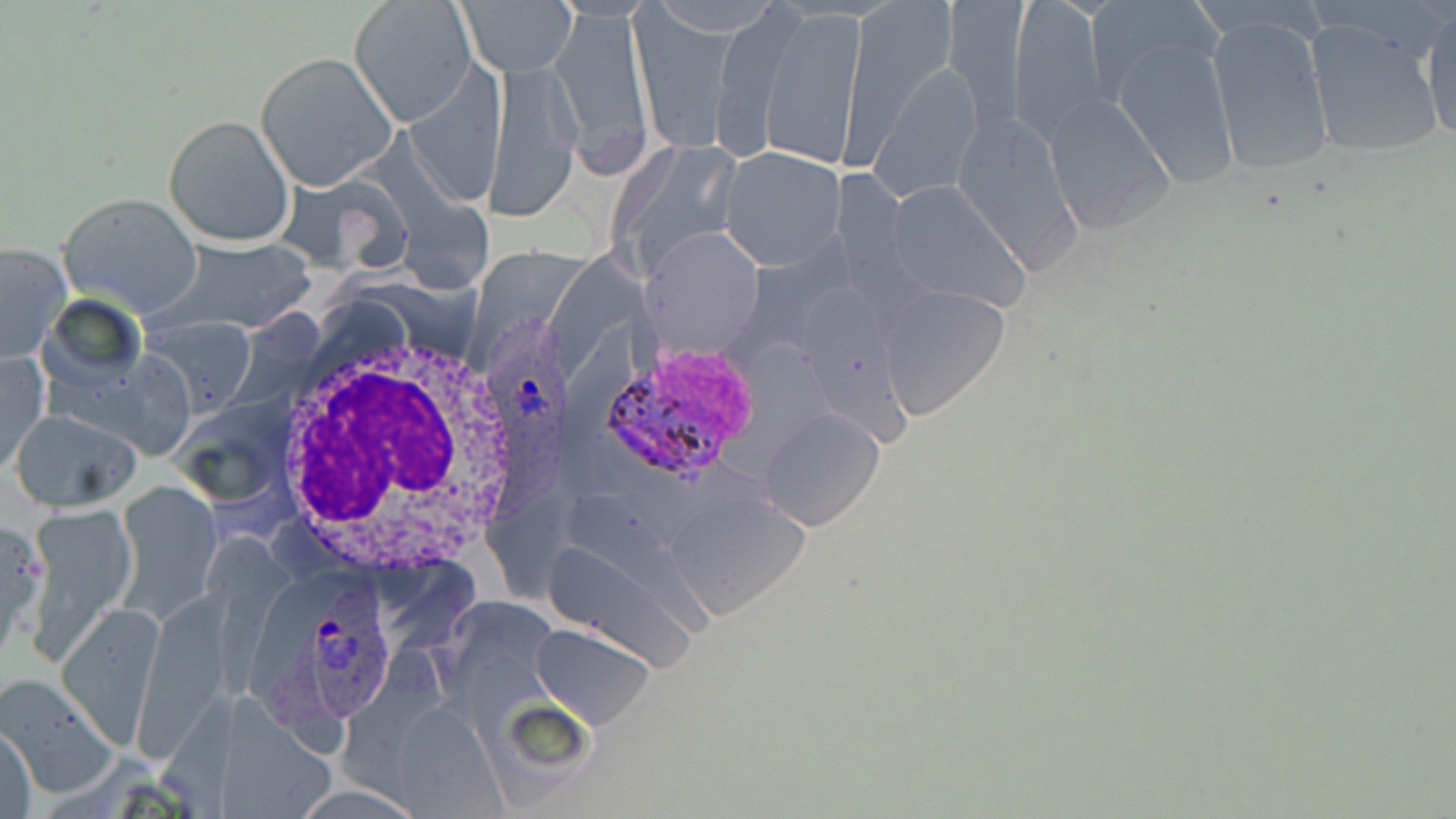
Approximate bounding boxes as (x1, y1, x2, y2) in pixels. Uninfected red blood cell locations: (844, 0, 963, 158), (1008, 0, 1113, 141), (1086, 0, 1222, 103), (348, 1, 476, 127), (461, 1, 574, 77), (943, 2, 1029, 117), (551, 4, 652, 169), (759, 7, 867, 167), (1420, 9, 1456, 146), (630, 10, 733, 155), (1205, 14, 1336, 178), (1301, 17, 1445, 163), (1112, 39, 1240, 189), (256, 53, 396, 190), (487, 58, 583, 219), (872, 61, 982, 202), (1041, 93, 1176, 236), (947, 108, 1085, 271), (163, 114, 295, 247), (609, 134, 751, 277), (715, 147, 847, 270), (884, 181, 1029, 310), (57, 192, 203, 318), (166, 238, 317, 331), (0, 242, 70, 363), (879, 285, 1011, 420), (142, 316, 254, 414), (1, 351, 48, 474), (762, 408, 884, 531), (13, 410, 142, 510), (118, 484, 221, 616), (669, 491, 811, 620), (24, 505, 136, 658), (59, 599, 163, 743), (531, 622, 656, 730), (1, 673, 116, 796), (389, 703, 504, 815), (1, 724, 37, 817), (293, 781, 415, 817). Plasmodium ovale-infected red blood cell locations: (484, 311, 573, 530), (591, 340, 761, 484), (253, 575, 389, 734). White blood cell locations: (265, 320, 531, 572). Slide-level diagnosis: Plasmodium ovale. May-Grünwald-Giemsa-stained preparation. Image is 1456×819 pixels. Thin blood smear. Captured at 1000x magnification. Single field of view. Light microscopy.